Mark where platelets are.
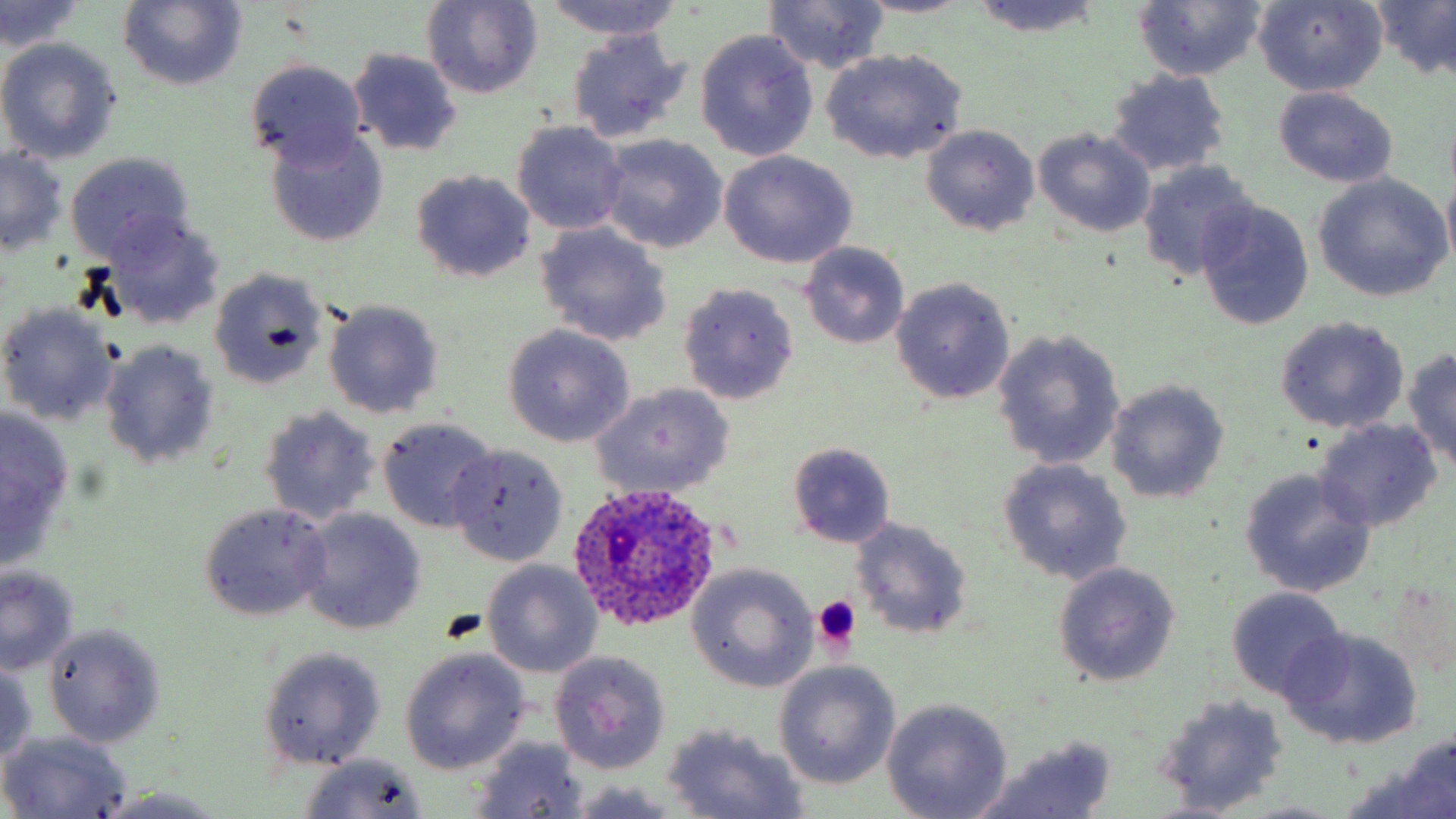

Approximate bounding boxes as named x1/y1/x2/y2 corners in pixels.
Platelets: (x1=813, y1=594, x2=860, y2=652).

Plasmodium ovale-infected red blood cell locations: (x1=570, y1=483, x2=727, y2=635). Uninfected red blood cell locations: (x1=854, y1=0, x2=974, y2=18), (x1=1370, y1=0, x2=1456, y2=82), (x1=1, y1=1, x2=84, y2=55), (x1=120, y1=1, x2=246, y2=91), (x1=422, y1=1, x2=543, y2=100), (x1=538, y1=1, x2=691, y2=41), (x1=966, y1=1, x2=1105, y2=38), (x1=1134, y1=1, x2=1265, y2=82), (x1=765, y1=2, x2=890, y2=74), (x1=1253, y1=3, x2=1386, y2=95), (x1=566, y1=29, x2=691, y2=146), (x1=695, y1=29, x2=818, y2=161), (x1=0, y1=40, x2=124, y2=165), (x1=348, y1=49, x2=463, y2=157), (x1=820, y1=50, x2=966, y2=163), (x1=244, y1=60, x2=370, y2=171), (x1=1106, y1=70, x2=1230, y2=178), (x1=1273, y1=86, x2=1398, y2=187), (x1=510, y1=120, x2=629, y2=235), (x1=921, y1=124, x2=1039, y2=237), (x1=265, y1=127, x2=388, y2=248), (x1=1034, y1=128, x2=1155, y2=238), (x1=596, y1=134, x2=728, y2=254), (x1=1045, y1=145, x2=1236, y2=263), (x1=0, y1=146, x2=69, y2=256), (x1=720, y1=151, x2=857, y2=269), (x1=66, y1=153, x2=195, y2=262), (x1=1137, y1=159, x2=1257, y2=283), (x1=410, y1=170, x2=536, y2=284), (x1=1442, y1=170, x2=1456, y2=271), (x1=1313, y1=175, x2=1452, y2=302), (x1=1195, y1=198, x2=1314, y2=329), (x1=104, y1=214, x2=226, y2=331), (x1=535, y1=223, x2=673, y2=346), (x1=799, y1=242, x2=911, y2=348), (x1=207, y1=268, x2=329, y2=390), (x1=890, y1=277, x2=1015, y2=405), (x1=676, y1=283, x2=800, y2=405), (x1=324, y1=299, x2=444, y2=419), (x1=0, y1=302, x2=119, y2=426), (x1=1274, y1=316, x2=1409, y2=434), (x1=503, y1=324, x2=635, y2=447), (x1=991, y1=328, x2=1125, y2=471), (x1=97, y1=339, x2=221, y2=471), (x1=1403, y1=349, x2=1456, y2=470), (x1=1106, y1=379, x2=1229, y2=504), (x1=588, y1=381, x2=736, y2=499), (x1=257, y1=405, x2=380, y2=526), (x1=0, y1=406, x2=76, y2=566), (x1=378, y1=416, x2=500, y2=533), (x1=1313, y1=418, x2=1441, y2=533), (x1=785, y1=441, x2=896, y2=548), (x1=446, y1=445, x2=569, y2=567), (x1=997, y1=459, x2=1132, y2=585), (x1=1240, y1=466, x2=1378, y2=599), (x1=197, y1=501, x2=334, y2=622), (x1=298, y1=508, x2=428, y2=635), (x1=849, y1=518, x2=972, y2=638), (x1=482, y1=560, x2=603, y2=678), (x1=1052, y1=561, x2=1181, y2=687), (x1=687, y1=563, x2=820, y2=693), (x1=0, y1=564, x2=79, y2=676), (x1=1224, y1=586, x2=1350, y2=702), (x1=41, y1=622, x2=166, y2=748), (x1=1280, y1=628, x2=1422, y2=750), (x1=258, y1=646, x2=388, y2=768), (x1=399, y1=647, x2=531, y2=774), (x1=549, y1=650, x2=671, y2=774), (x1=0, y1=658, x2=39, y2=765), (x1=774, y1=662, x2=899, y2=788), (x1=1154, y1=694, x2=1291, y2=812), (x1=882, y1=698, x2=1011, y2=818), (x1=660, y1=724, x2=809, y2=818), (x1=1, y1=731, x2=132, y2=817), (x1=971, y1=736, x2=1119, y2=819), (x1=469, y1=737, x2=591, y2=816), (x1=1353, y1=745, x2=1455, y2=818), (x1=294, y1=754, x2=432, y2=819), (x1=566, y1=781, x2=691, y2=818), (x1=94, y1=786, x2=233, y2=818). Slide-level diagnosis: Plasmodium ovale. Thin blood film. Single field of view. May-Grünwald-Giemsa-stained preparation. Optical microscopy. Captured at 1000x magnification. Image is 1456×819 pixels.